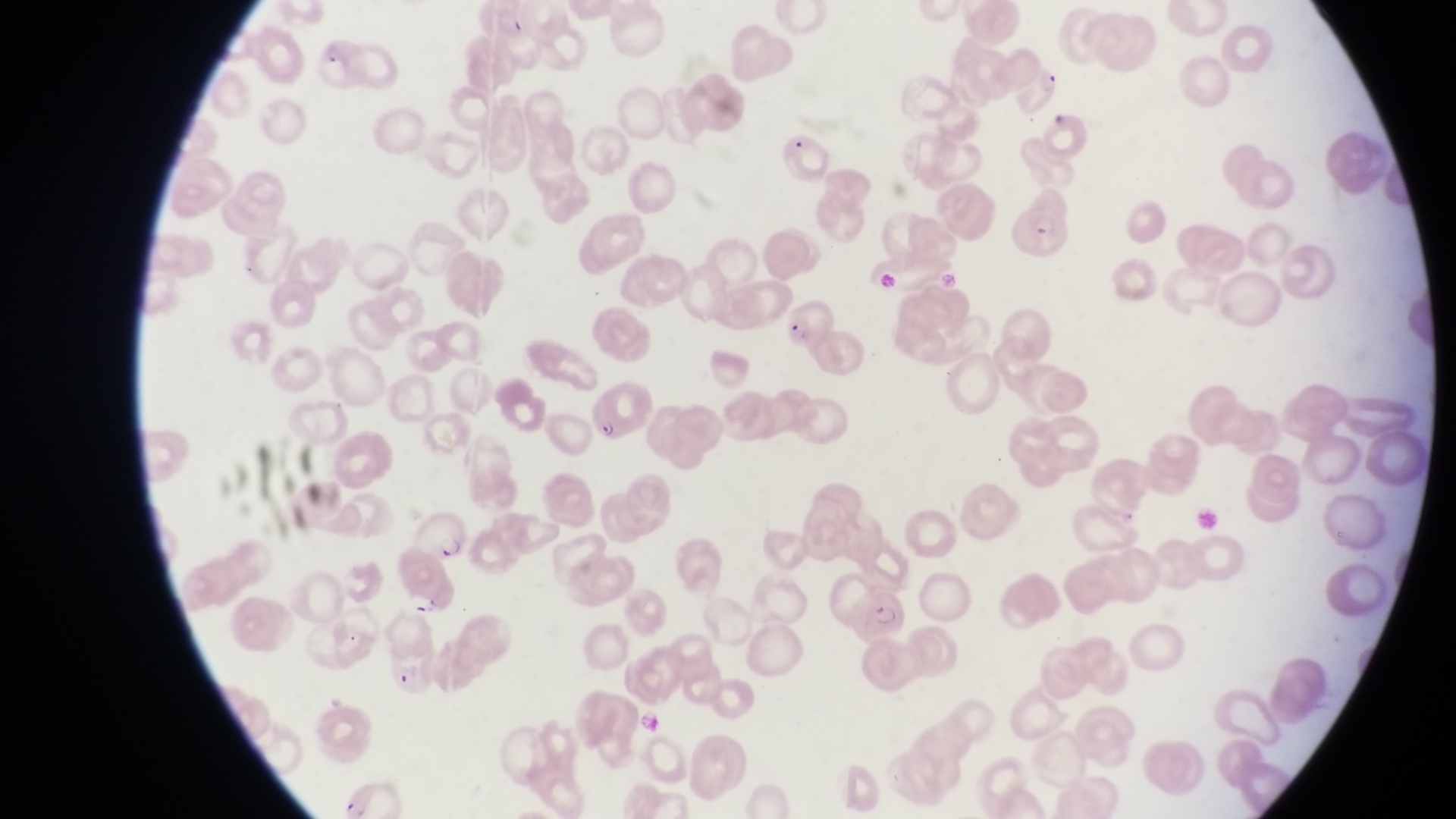
Approximate bounding boxes as left top right bottom in pixels. Parasitised red blood cell locations: 312 32 364 95; 1012 58 1061 117; 1012 204 1079 265; 770 297 837 353; 587 383 656 446; 412 510 468 560; 393 565 460 620; 843 585 904 635; 384 653 436 706. Photographed through the eyepiece of an Olympus CX-23 microscope with a smartphone camera. Single field of view. Collected in Uganda. At a magnification of 1000x. Thin blood film. Image is 1456×819 pixels.